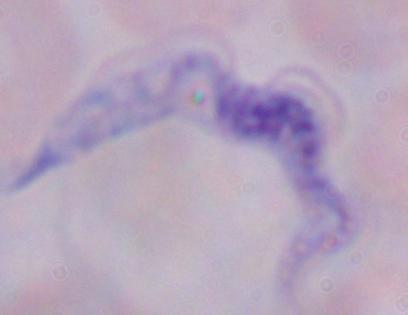

identification = trypanosome
modality = micrograph
magnification = 1000x